Name the blood parasite species.
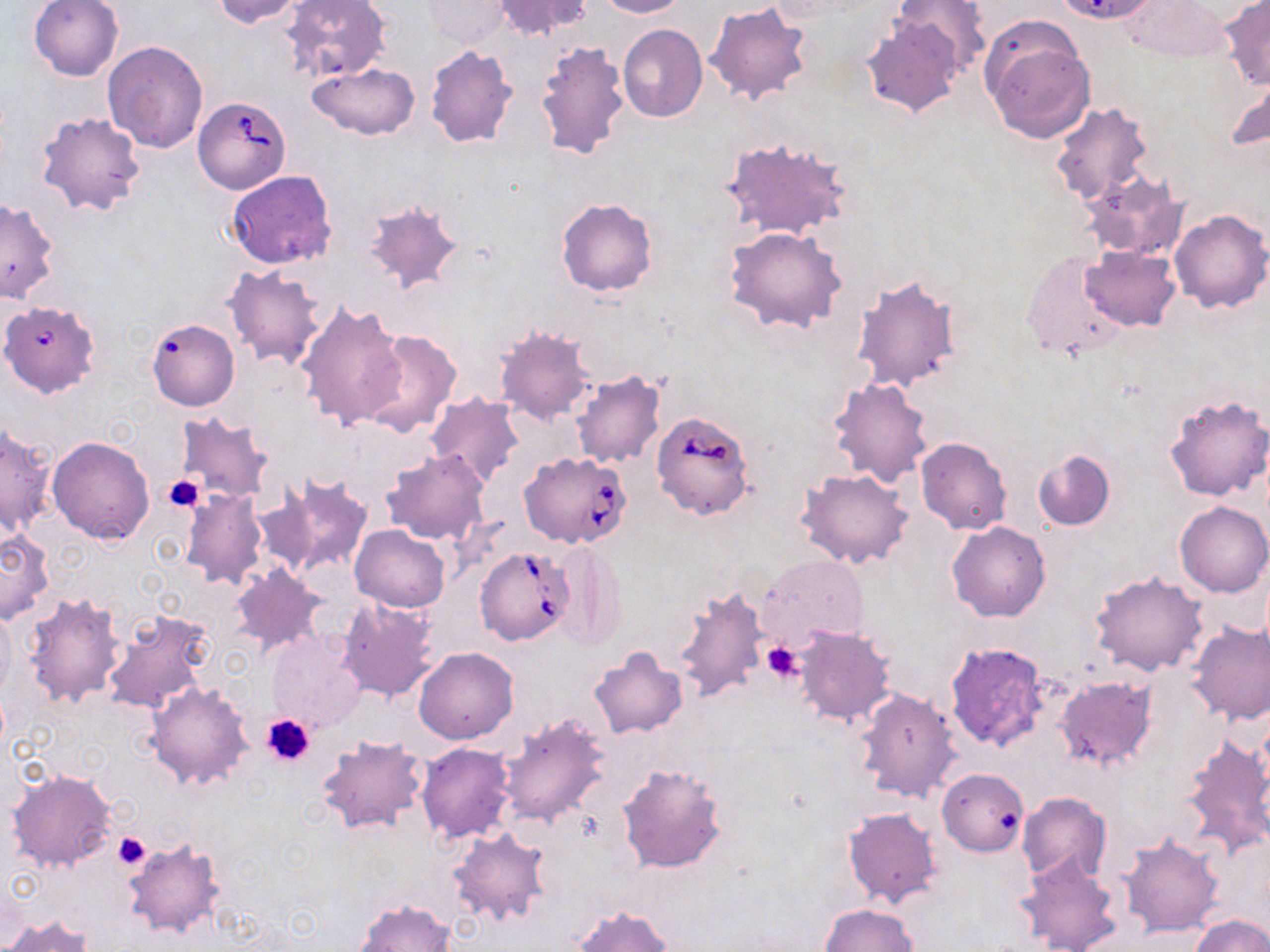

Babesia divergens.

Approximate bounding boxes as named x1/y1/x2/y2 corners in pixels. Platelet locations: (x1=162, y1=475, x2=206, y2=512), (x1=763, y1=641, x2=805, y2=683), (x1=262, y1=711, x2=317, y2=767), (x1=113, y1=831, x2=151, y2=870). Uninfected red blood cell locations: (x1=28, y1=0, x2=123, y2=81), (x1=211, y1=0, x2=311, y2=28), (x1=491, y1=0, x2=593, y2=40), (x1=595, y1=0, x2=686, y2=18), (x1=1121, y1=0, x2=1235, y2=62), (x1=282, y1=1, x2=391, y2=82), (x1=423, y1=1, x2=509, y2=47), (x1=889, y1=1, x2=990, y2=78), (x1=1220, y1=1, x2=1270, y2=90), (x1=704, y1=3, x2=812, y2=106), (x1=862, y1=16, x2=967, y2=118), (x1=979, y1=22, x2=1095, y2=145), (x1=618, y1=25, x2=707, y2=122), (x1=536, y1=38, x2=631, y2=162), (x1=101, y1=41, x2=209, y2=154), (x1=424, y1=46, x2=518, y2=149), (x1=307, y1=63, x2=418, y2=140), (x1=1227, y1=72, x2=1270, y2=158), (x1=1051, y1=102, x2=1153, y2=207), (x1=34, y1=111, x2=146, y2=217), (x1=718, y1=136, x2=853, y2=240), (x1=225, y1=170, x2=336, y2=270), (x1=1080, y1=171, x2=1187, y2=261), (x1=0, y1=197, x2=59, y2=302), (x1=362, y1=198, x2=466, y2=297), (x1=557, y1=199, x2=656, y2=297), (x1=1168, y1=208, x2=1269, y2=313), (x1=723, y1=227, x2=849, y2=334), (x1=1079, y1=244, x2=1181, y2=331), (x1=1020, y1=252, x2=1131, y2=360), (x1=223, y1=264, x2=328, y2=370), (x1=852, y1=275, x2=961, y2=393), (x1=0, y1=300, x2=101, y2=396), (x1=296, y1=301, x2=408, y2=433), (x1=146, y1=318, x2=240, y2=411), (x1=494, y1=326, x2=598, y2=426), (x1=356, y1=328, x2=463, y2=438), (x1=569, y1=370, x2=667, y2=469), (x1=829, y1=377, x2=934, y2=488), (x1=1164, y1=392, x2=1269, y2=502), (x1=426, y1=393, x2=523, y2=487), (x1=174, y1=413, x2=274, y2=505), (x1=1, y1=422, x2=55, y2=536), (x1=48, y1=436, x2=154, y2=543), (x1=916, y1=437, x2=1012, y2=534), (x1=381, y1=448, x2=490, y2=545), (x1=1031, y1=448, x2=1116, y2=531), (x1=795, y1=469, x2=914, y2=570), (x1=261, y1=472, x2=374, y2=580), (x1=177, y1=489, x2=267, y2=592), (x1=1175, y1=502, x2=1269, y2=598), (x1=947, y1=521, x2=1050, y2=621), (x1=350, y1=524, x2=450, y2=612), (x1=0, y1=529, x2=54, y2=622), (x1=552, y1=541, x2=625, y2=648), (x1=759, y1=555, x2=870, y2=648), (x1=229, y1=562, x2=329, y2=655), (x1=1090, y1=570, x2=1208, y2=676), (x1=673, y1=583, x2=771, y2=706), (x1=21, y1=591, x2=126, y2=709), (x1=338, y1=598, x2=440, y2=700), (x1=0, y1=605, x2=16, y2=700), (x1=98, y1=608, x2=211, y2=716), (x1=1187, y1=621, x2=1270, y2=726), (x1=792, y1=627, x2=895, y2=728), (x1=267, y1=630, x2=365, y2=732), (x1=945, y1=641, x2=1050, y2=751), (x1=414, y1=646, x2=517, y2=743), (x1=589, y1=646, x2=688, y2=739), (x1=1054, y1=675, x2=1157, y2=772), (x1=145, y1=682, x2=254, y2=791), (x1=855, y1=688, x2=961, y2=803), (x1=496, y1=711, x2=611, y2=826), (x1=1181, y1=732, x2=1270, y2=856), (x1=316, y1=734, x2=429, y2=836), (x1=416, y1=742, x2=515, y2=842), (x1=616, y1=761, x2=729, y2=875), (x1=7, y1=769, x2=117, y2=873), (x1=937, y1=769, x2=1028, y2=856), (x1=1017, y1=791, x2=1111, y2=883), (x1=843, y1=807, x2=942, y2=909), (x1=449, y1=825, x2=553, y2=927), (x1=1117, y1=831, x2=1224, y2=937), (x1=122, y1=838, x2=226, y2=939), (x1=1017, y1=854, x2=1121, y2=952), (x1=356, y1=899, x2=456, y2=952), (x1=818, y1=904, x2=917, y2=951), (x1=574, y1=905, x2=672, y2=952), (x1=4, y1=914, x2=93, y2=952), (x1=1191, y1=914, x2=1270, y2=952). Babesia divergens-infected red blood cell locations: (x1=192, y1=95, x2=289, y2=193), (x1=650, y1=410, x2=756, y2=521), (x1=518, y1=451, x2=631, y2=548), (x1=476, y1=547, x2=575, y2=646). Light microscopy. Single field of view. 1000x magnification. May-Grünwald-Giemsa stain. Thin blood film. Image is 1270×952 pixels.